Report the malaria status of this cell.
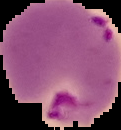

It is parasitized.

From a thin blood smear. Image is 121×130 pixels. Segmented cell region on a black background.